Point out each malaria parasite.
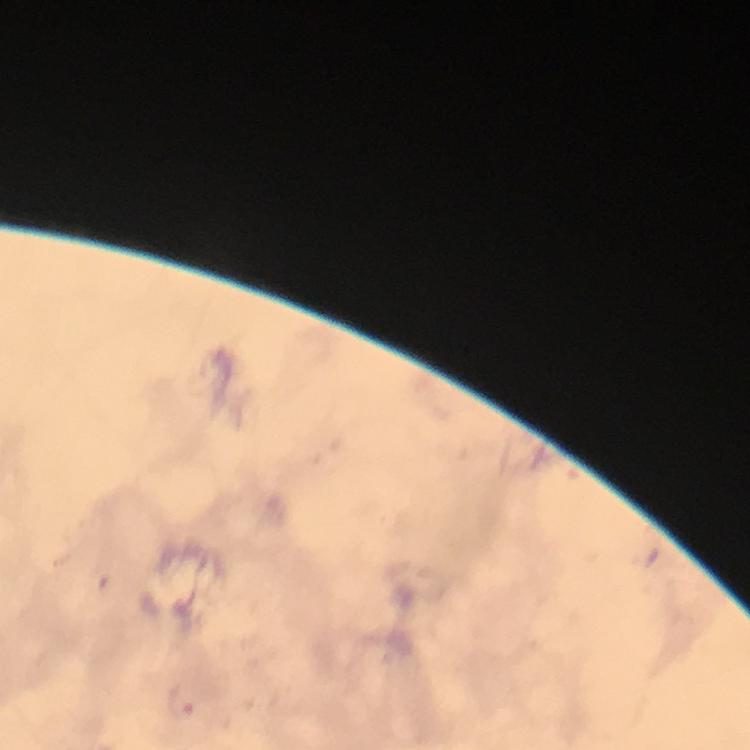
Approximate centers as [x, y] in pixels.
Malaria parasites: [181, 702].

Summary:
  - Immersion oil: used
  - Magnification: 100x
  - Cropped from: a single field of view
  - Context: from a malaria diagnostic workup
  - Stain: Giemsa
  - Capture: smartphone photograph through a microscope
  - Preparation: thick smear
  - Image size: 750×750 pixels